Report the malaria status of this cell.
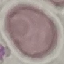
It is uninfected.

Summary:
  - Image type: automatically extracted cell patch, resized to 64 × 64 pixels
  - Preparation: thin blood smear
  - Stain: Giemsa
  - Capture: smartphone through the microscope eyepiece